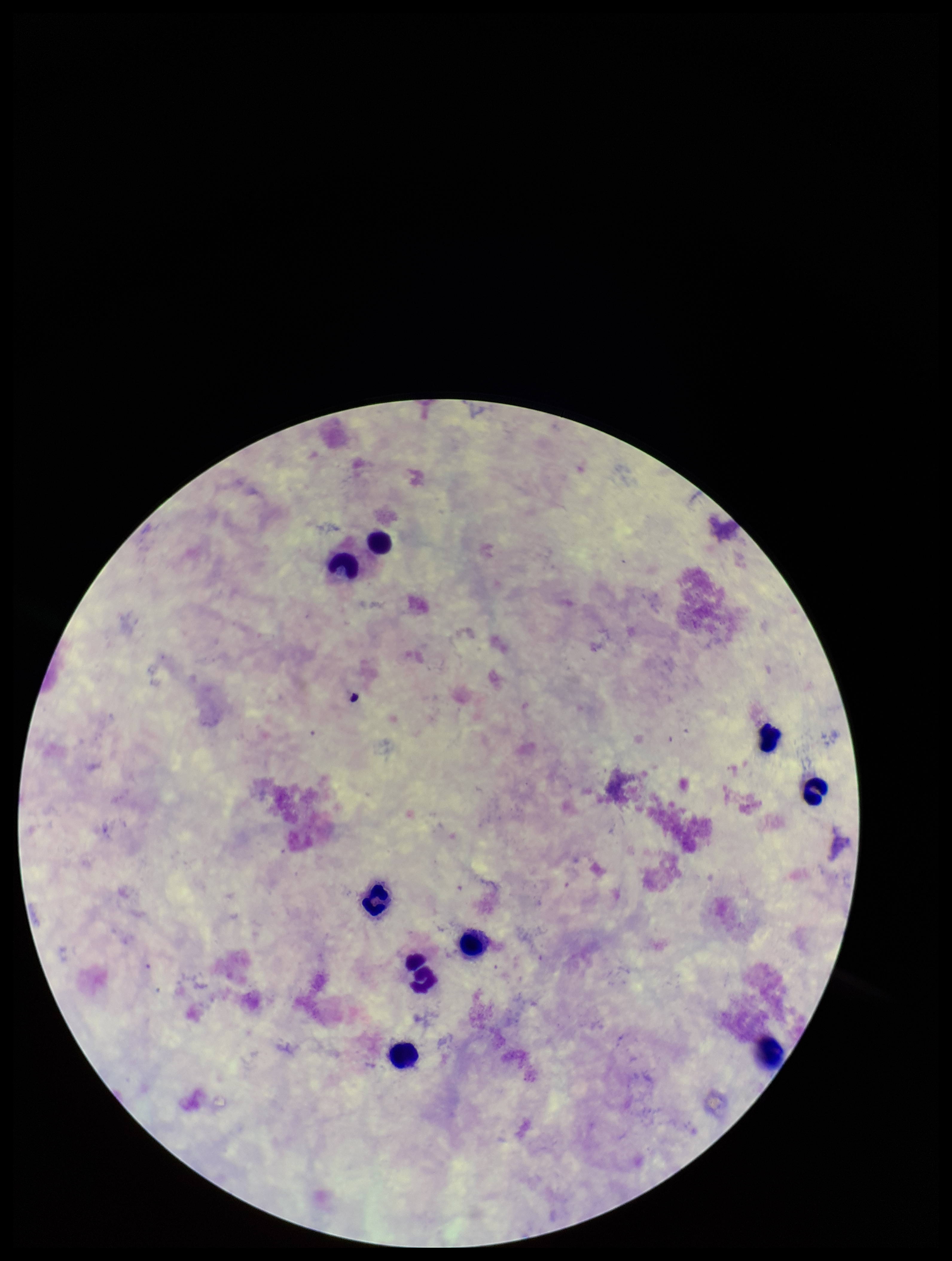

Summary:
  - Leukocyte count: 9
  - Image size: 952×1261 pixels
  - Patient malaria status: negative
  - Plasmodium parasites: none detected
  - Preparation: thick blood smear
  - Field of view: single
  - Stain: Giemsa
  - Capture: smartphone photograph through the microscope eyepiece
  - Parasite count: 0